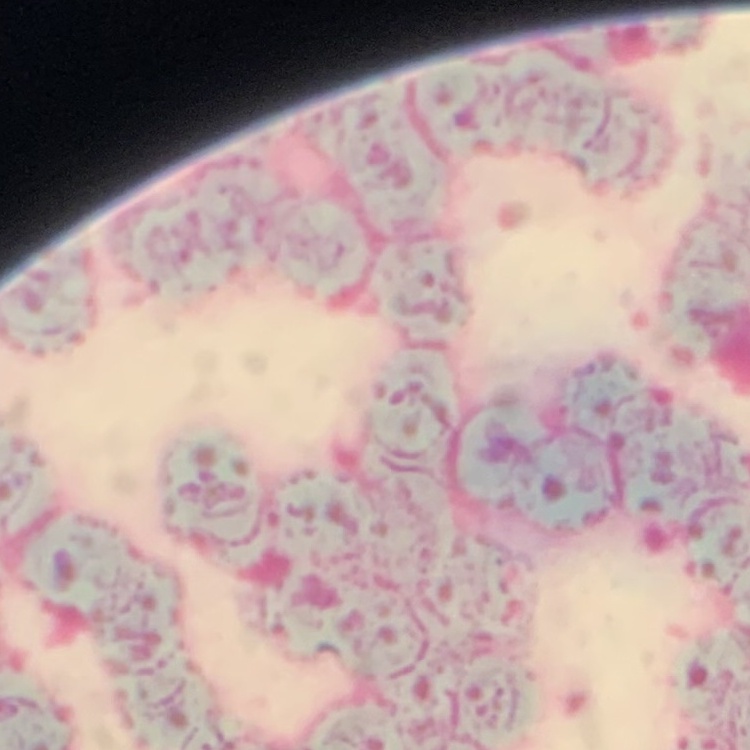
erythrocyte morphology = rouleaux formation
preparation = thin blood film
image type = square crop of a larger photomicrograph
stain = Field's or Giemsa